Locate every Plasmodium parasite.
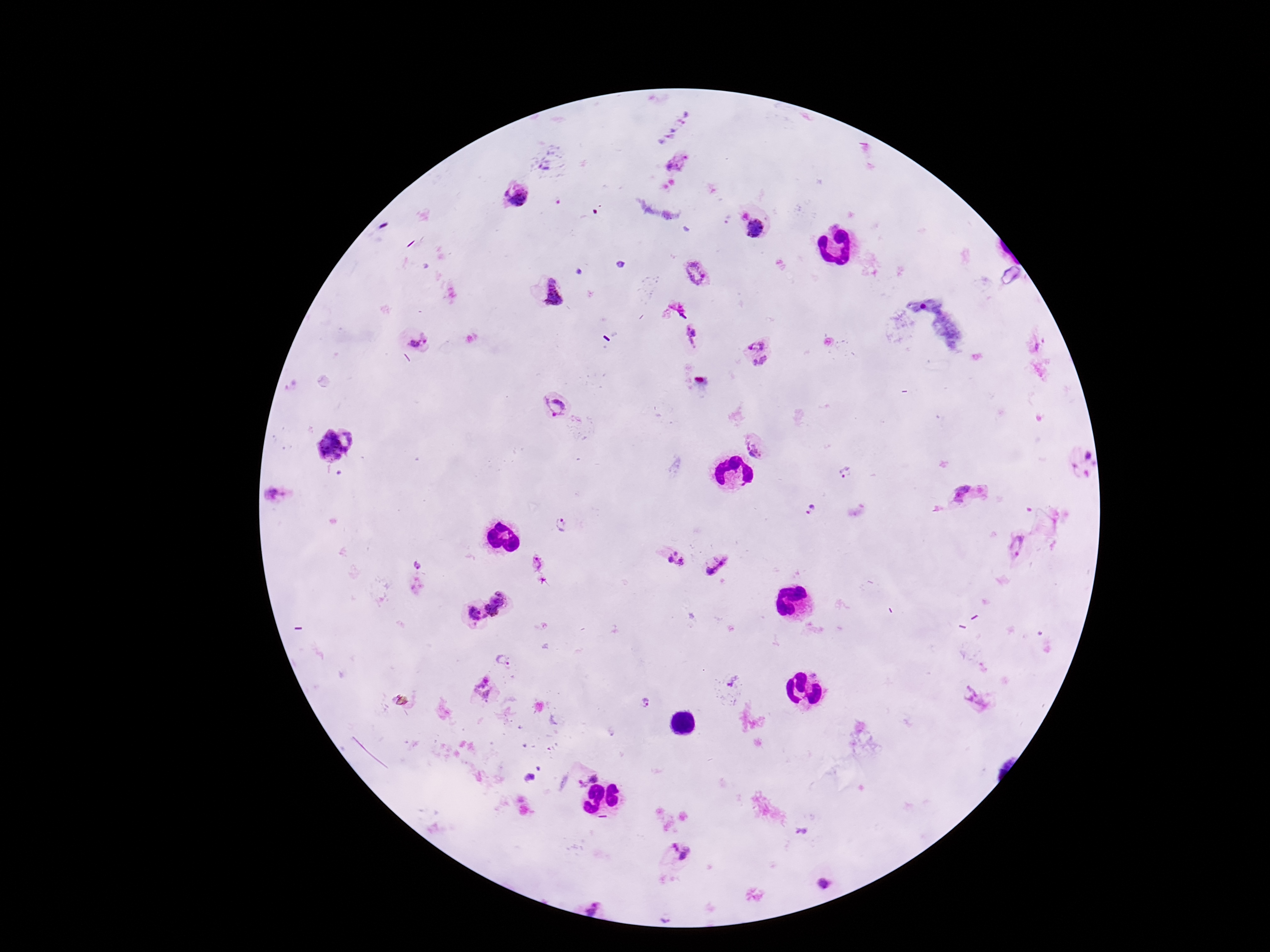

Approximate object centers, in pixels from the top-left corner.
Plasmodium parasites: (x=665, y=118), (x=548, y=162), (x=679, y=162), (x=516, y=196), (x=754, y=230), (x=696, y=273), (x=552, y=294), (x=690, y=335), (x=758, y=340), (x=420, y=343), (x=761, y=365), (x=559, y=406), (x=759, y=444), (x=334, y=447), (x=1083, y=463), (x=843, y=473), (x=277, y=493), (x=963, y=493), (x=813, y=511), (x=561, y=526), (x=1017, y=543), (x=674, y=559), (x=418, y=563), (x=538, y=564), (x=719, y=565), (x=500, y=596), (x=491, y=611), (x=472, y=615), (x=503, y=661), (x=732, y=682), (x=486, y=687), (x=977, y=700), (x=645, y=703), (x=594, y=777), (x=529, y=779), (x=581, y=785), (x=678, y=850), (x=824, y=885), (x=594, y=906).

Summary:
  - Stain: Giemsa
  - Field of view: one from this slide
  - Magnification: 100x
  - Image size: 1270×952 pixels
  - Capture: smartphone camera through the microscope eyepiece
  - Preparation: thick blood smear
  - Patient malaria status: positive